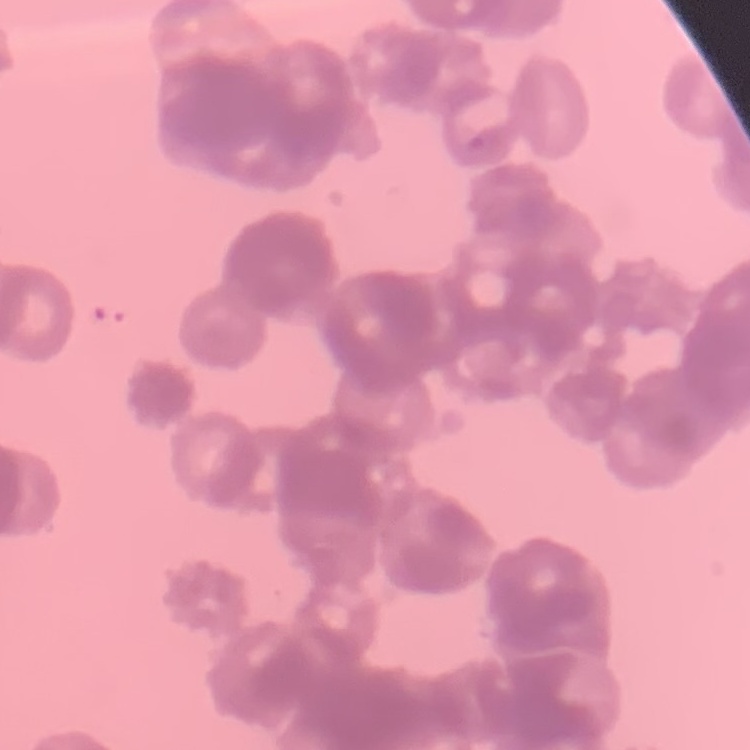
red blood cell morphology = rouleaux formation
image type = one tile cut from a larger photomicrograph
preparation = thin peripheral smear
stain = Field's or Giemsa